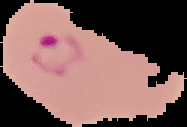

image type = cell region segmented out of the field of view; surrounding area masked to black
image size = 187×127 pixels
result = Plasmodium parasites detected
preparation = thin blood film